Assess the morphology of the erythrocytes.
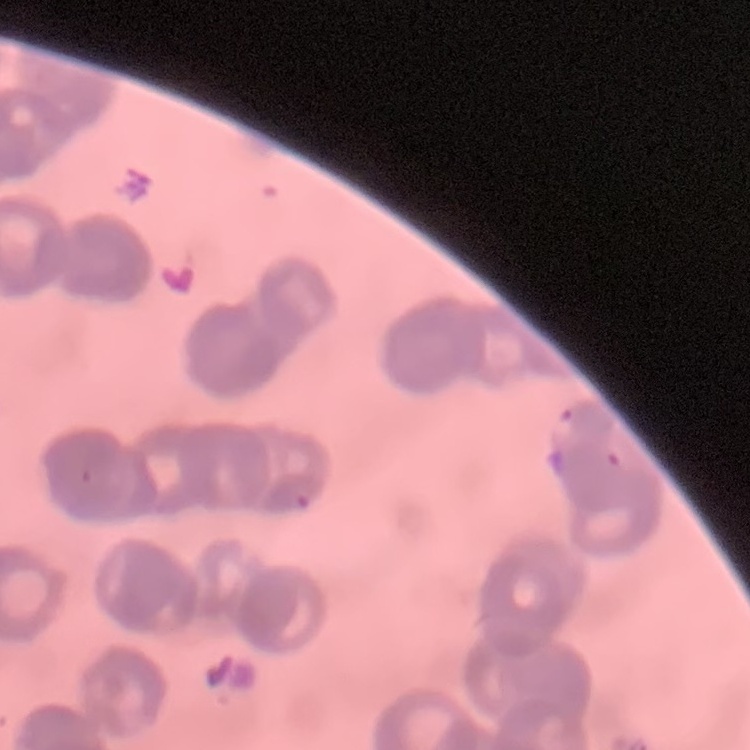
Rouleaux formation.

Summary:
  - Image type: one tile cut from a larger photomicrograph
  - Preparation: thin blood film
  - Stain: Field's or Giemsa